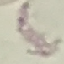

Summary:
  - Malaria status: uninfected
  - Stain: Giemsa
  - Image type: automatically extracted cell patch, resized to 64 × 64 pixels
  - Capture: smartphone camera at the microscope eyepiece
  - Preparation: thin blood smear